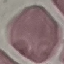
result: no malaria parasites seen
preparation: thin smear
capture: smartphone camera at the microscope eyepiece
image_type: cell patch, automatically extracted from a larger field of view and resized to 64 × 64 pixels
stain: Giemsa